Outline platelets.
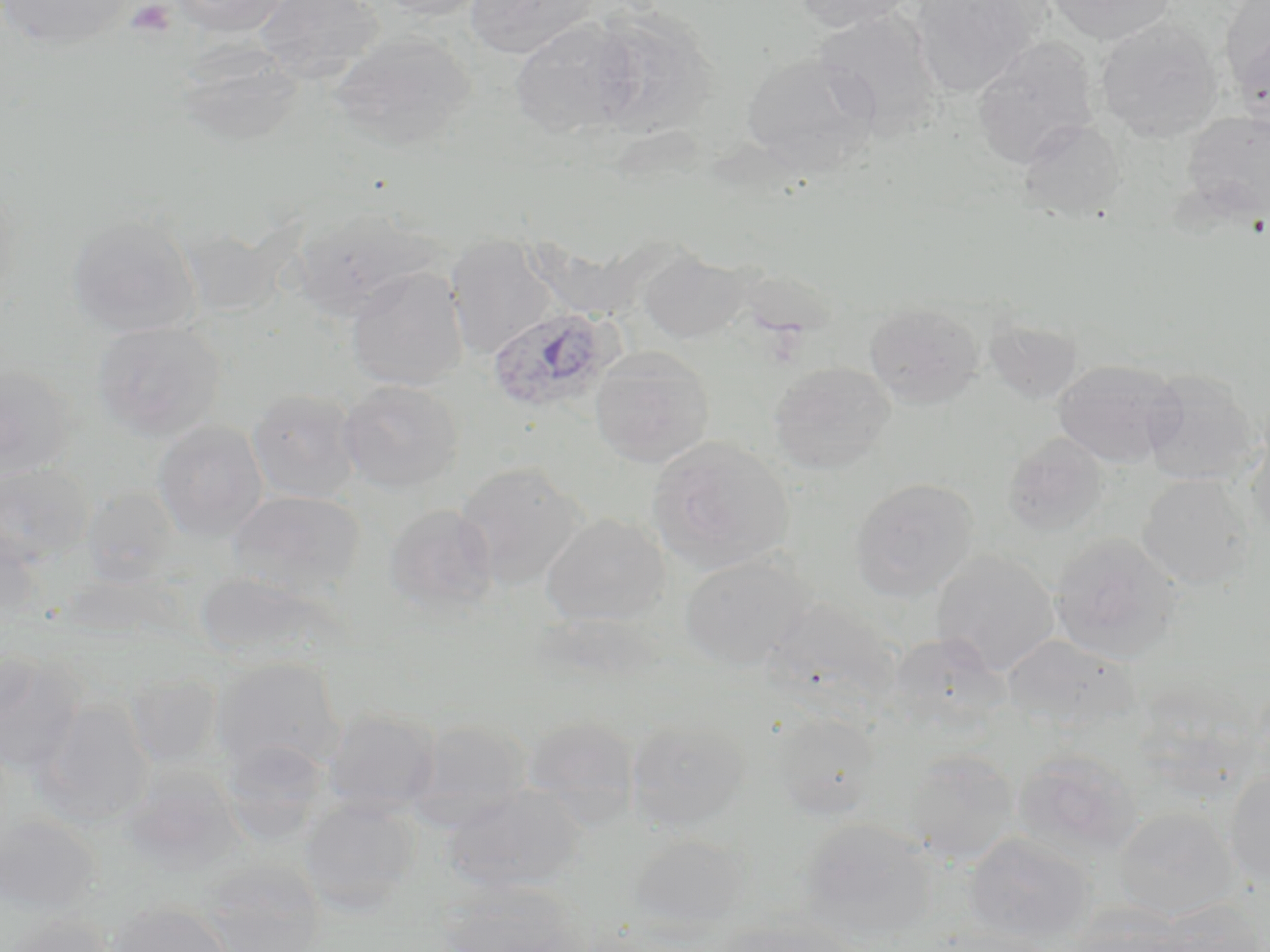
Approximate bounding boxes as (x1, y1, x2, y2) in pixels.
Platelets: (125, 1, 177, 38).

Summary:
  - Uninfected red blood cell locations: (0, 0, 134, 51), (170, 0, 290, 37), (254, 0, 384, 81), (371, 0, 491, 20), (465, 0, 600, 59), (794, 0, 919, 33), (909, 0, 1040, 96), (1046, 0, 1176, 45), (1221, 0, 1270, 104), (587, 9, 718, 138), (812, 10, 944, 137), (1095, 18, 1223, 142), (509, 21, 636, 139), (329, 31, 477, 153), (971, 37, 1099, 169), (174, 38, 303, 147), (741, 52, 877, 173), (1182, 110, 1270, 222), (1017, 118, 1126, 220), (292, 204, 439, 321), (66, 213, 202, 337), (177, 222, 288, 317), (444, 235, 560, 359), (637, 250, 748, 344), (346, 267, 468, 391), (864, 301, 985, 408), (984, 313, 1084, 404), (92, 320, 226, 441), (589, 347, 715, 468), (1052, 358, 1184, 467), (768, 361, 894, 476), (0, 363, 78, 480), (1141, 369, 1259, 486), (338, 379, 464, 494), (247, 388, 362, 503), (152, 420, 267, 540), (1243, 430, 1270, 543), (1002, 432, 1109, 537), (647, 436, 794, 572), (0, 461, 94, 566), (454, 462, 587, 590), (1137, 474, 1251, 589), (850, 477, 979, 601), (82, 487, 181, 587), (227, 490, 365, 598), (383, 503, 499, 616), (540, 513, 671, 626), (0, 530, 45, 630), (1049, 532, 1183, 663), (931, 551, 1059, 676), (678, 553, 814, 670), (194, 572, 343, 669), (767, 596, 901, 711), (886, 632, 1012, 737), (1002, 634, 1137, 732), (0, 651, 86, 778), (211, 657, 346, 778), (125, 673, 223, 767), (35, 700, 154, 826), (321, 707, 442, 818), (771, 710, 883, 820), (520, 715, 641, 826), (625, 717, 750, 832), (404, 718, 534, 831), (221, 740, 333, 846), (903, 748, 1020, 865), (1011, 749, 1143, 863), (119, 767, 245, 876), (1223, 767, 1270, 888), (441, 783, 585, 893), (298, 797, 420, 917), (1113, 807, 1239, 922), (0, 813, 100, 915), (800, 817, 937, 944), (964, 831, 1096, 946), (628, 834, 751, 932), (197, 860, 327, 952), (435, 878, 587, 952), (105, 900, 233, 952), (1148, 900, 1267, 952), (1064, 903, 1192, 952), (3, 913, 117, 952), (711, 916, 866, 952)
  - Plasmodium ovale-infected red blood cell locations: (485, 305, 618, 415)
  - Slide-level diagnosis: Plasmodium ovale
  - Image size: 1270×952 pixels
  - Stain: May-Grünwald-Giemsa
  - Modality: light microscopy
  - Magnification: 1000x
  - Preparation: thin blood smear
  - Field of view: one of a larger specimen